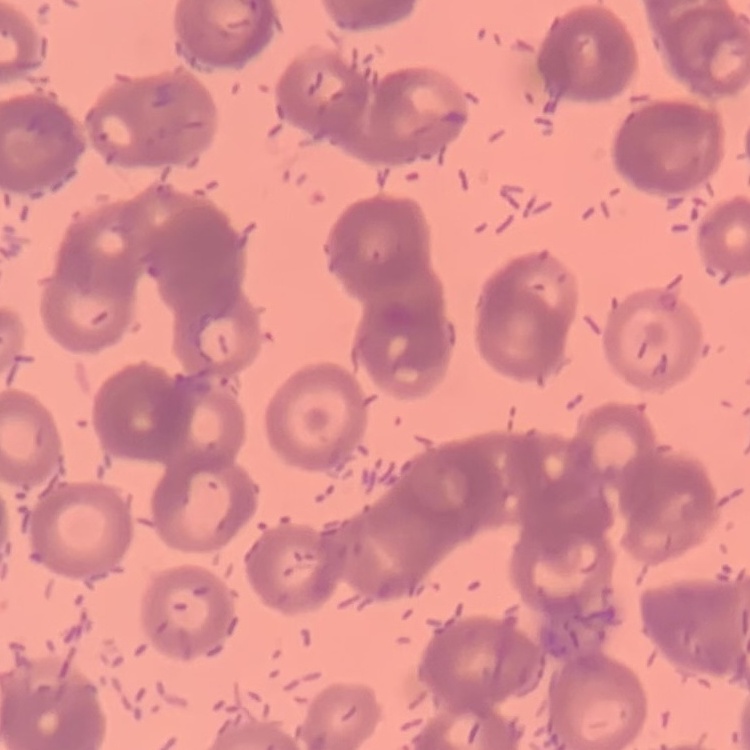
Summary:
  - Red blood cell morphology: rouleaux formation
  - Image type: square crop of a larger photomicrograph
  - Stain: Field's or Giemsa
  - Preparation: thin blood smear